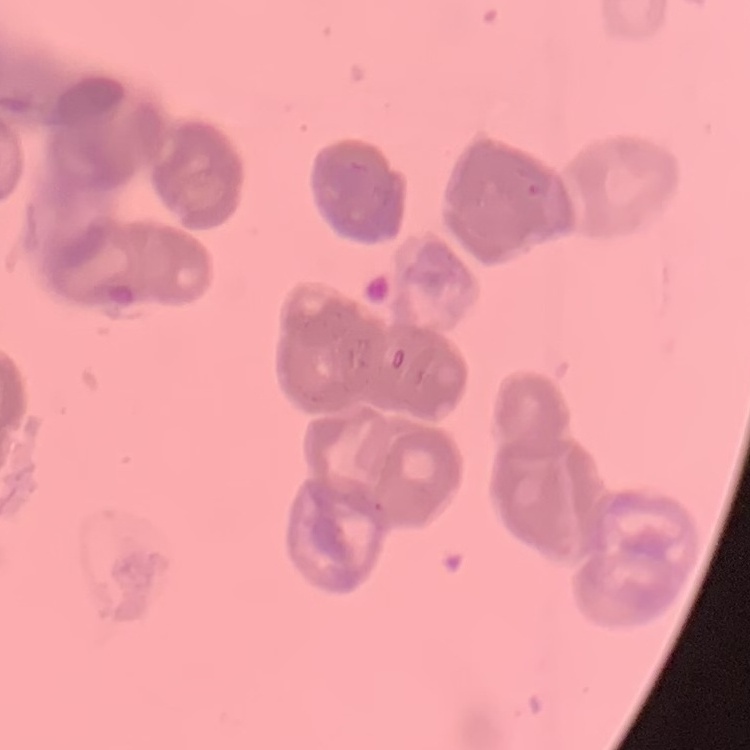

The erythrocytes exhibit rouleaux formation. Field's or Giemsa stain. Thin peripheral smear. Square crop of a larger photomicrograph.